Classify this cell by malaria status.
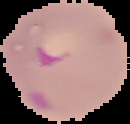
It is parasitized.

image type = segmented cell region with the area outside set to black
preparation = thin blood smear
image size = 130×124 pixels